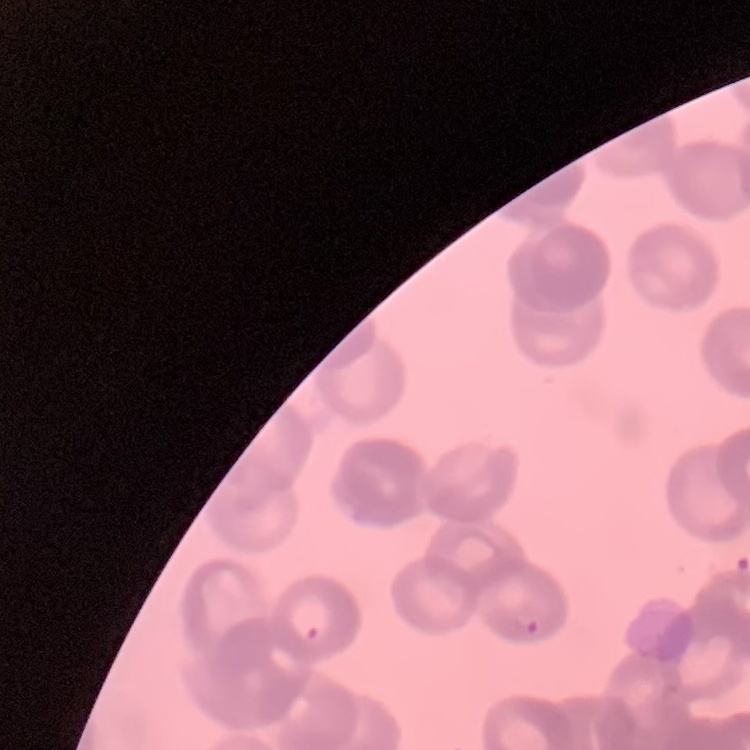
Summary:
  - Red blood cell morphology: rouleaux formation
  - Preparation: thin peripheral smear
  - Stain: Field's or Giemsa
  - Image type: square crop of a larger photomicrograph